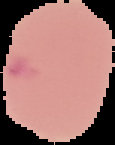

Cell region segmented out of the field of view; the surrounding area is masked to black. Image is 115×145 pixels. Result: negative for malaria parasites. From a thin blood film.